Report the malaria status of this cell.
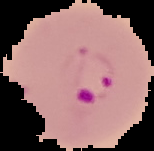
Parasitized.

image size = 154×151 pixels
image type = segmented cell region on a black background
preparation = thin blood smear